Locate every Plasmodium parasite.
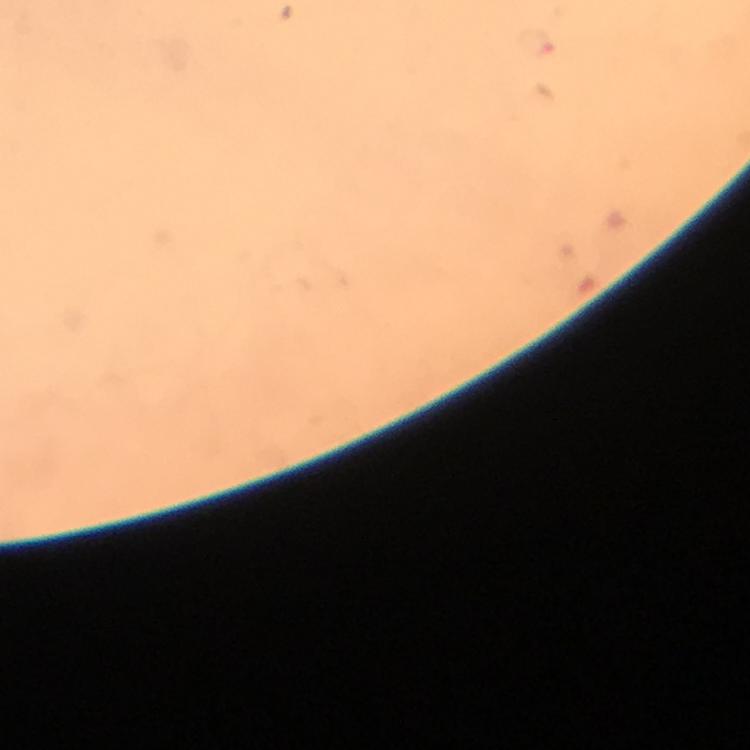
Approximate object centers, in pixels from the top-left corner.
Plasmodium parasites: (x=537, y=42).

Summary:
  - Capture: smartphone mounted on the microscope
  - Immersion oil: used
  - Image size: 750×750 pixels
  - Context: from a malaria diagnostic workup
  - Magnification: 100x
  - Cropped from: a single field of view
  - Preparation: thick blood smear
  - Stain: Giemsa